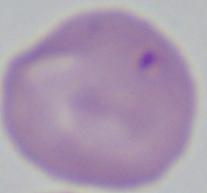
magnification: 1000x
identification: Babesia
modality: micrograph